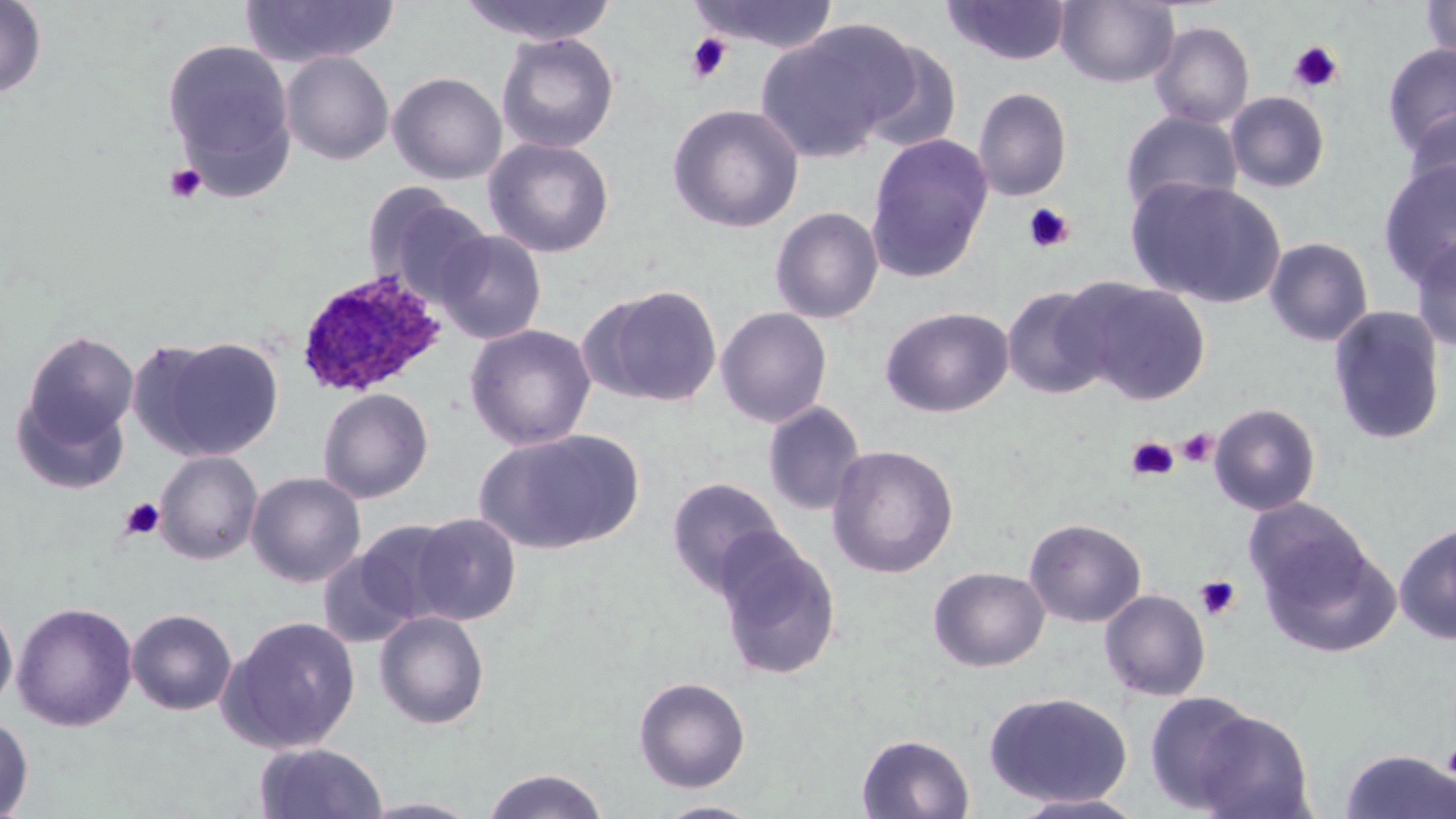
Summary:
  - Coordinate format: approximate bounding boxes as (x1,y1)-(x2,y2) corner pairs in pixels
  - Uninfected red blood cell locations: (0,0)-(47,99), (458,0)-(619,45), (1056,0)-(1179,87), (1420,0)-(1455,64), (240,1)-(400,68), (686,1)-(841,54), (943,1)-(1071,66), (1150,21)-(1255,129), (756,25)-(904,163), (496,33)-(620,153), (162,39)-(295,183), (855,40)-(963,152), (1381,44)-(1456,158), (281,51)-(394,165), (388,72)-(507,184), (973,87)-(1072,202), (1225,91)-(1330,193), (667,104)-(804,233), (1402,109)-(1456,212), (1119,110)-(1243,215), (865,133)-(994,282), (483,137)-(615,258), (1376,159)-(1456,290), (1129,178)-(1286,308), (364,186)-(492,306), (770,206)-(884,324), (433,229)-(547,345), (1410,231)-(1456,353), (1264,237)-(1374,347), (1072,280)-(1212,405), (585,284)-(724,408), (1001,285)-(1116,400), (716,306)-(832,427), (879,306)-(1014,418), (1328,306)-(1447,446), (464,324)-(597,450), (21,330)-(139,445), (139,337)-(285,461), (318,387)-(433,503), (11,388)-(130,495), (763,402)-(866,516), (1209,402)-(1321,515), (474,429)-(643,556), (826,444)-(959,578), (154,451)-(263,565), (246,471)-(366,587), (666,477)-(787,597), (1243,498)-(1373,615), (409,512)-(522,625), (1024,518)-(1146,627), (356,519)-(463,622), (1395,520)-(1456,645), (1259,534)-(1402,659), (712,536)-(843,680), (317,548)-(419,648), (929,567)-(1050,672), (1099,589)-(1211,701), (12,601)-(138,731), (0,602)-(18,717), (126,608)-(238,715), (374,610)-(490,729), (220,615)-(362,753), (632,676)-(751,793), (983,691)-(1132,807), (1144,691)-(1263,814), (1188,707)-(1316,819), (0,715)-(34,817), (856,733)-(975,819), (255,742)-(388,819), (1338,748)-(1456,819), (481,768)-(609,818), (1010,792)-(1150,818), (359,797)-(484,818), (649,800)-(767,818)
  - Platelet locations: (685,33)-(733,83), (1288,39)-(1345,94), (164,163)-(207,204), (1023,203)-(1074,254), (1177,428)-(1217,468), (1126,436)-(1178,481), (119,497)-(165,542), (1195,575)-(1241,621), (1441,744)-(1455,777)
  - Plasmodium ovale-infected red blood cell locations: (294,270)-(447,399)
  - Slide-level diagnosis: Plasmodium ovale
  - Field of view: one of a larger specimen
  - Stain: May-Grünwald-Giemsa
  - Magnification: 1000x
  - Modality: light microscopy
  - Image size: 1456×819 pixels
  - Preparation: thin blood smear